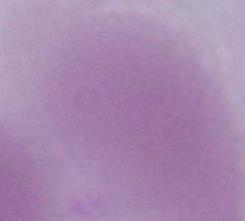

identification = red blood cell
magnification = 1000x
modality = photomicrograph